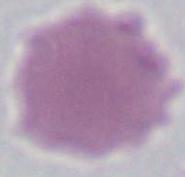

Photomicrograph. 1000x magnification. An erythrocyte is seen.